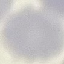

Summary:
  - Malaria status: uninfected
  - Image type: automatically extracted cell patch, resized to 64 × 64 pixels
  - Preparation: thin blood smear
  - Capture: smartphone camera at the microscope eyepiece
  - Stain: Giemsa